Point out Plasmodium parasites and leukocytes.
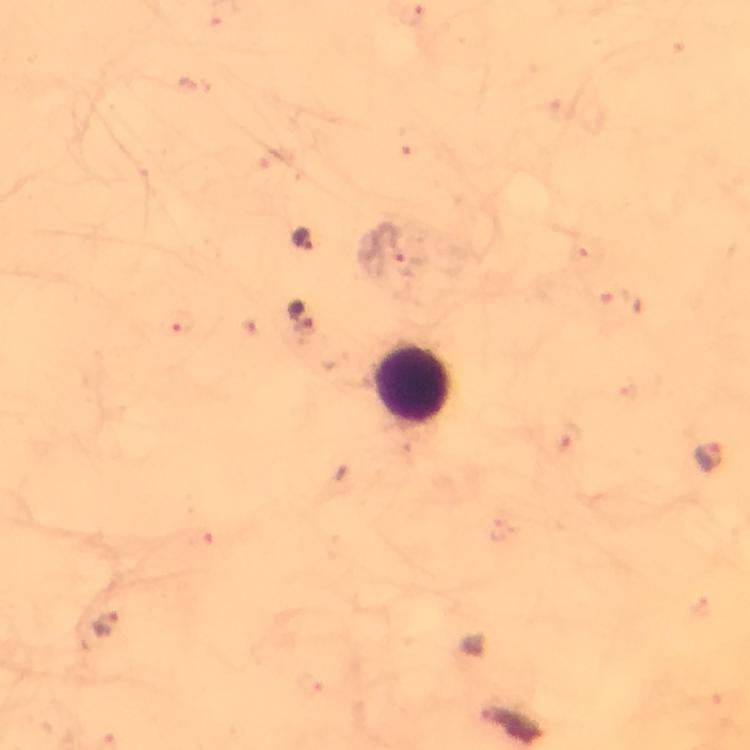
Approximate centers as {x, y} in pixels.
Plasmodium parasites: {304, 239}, {304, 318}, {710, 459}, {106, 624}.
Leukocytes: {414, 382}.

{
  "immersion_oil": "used",
  "context": "from a malaria diagnostic workup",
  "magnification": "100x",
  "preparation": "thick blood smear",
  "image_size": "750×750 pixels",
  "stain": "Giemsa",
  "cropped_from": "one field of view",
  "capture": "smartphone mounted on the microscope"
}